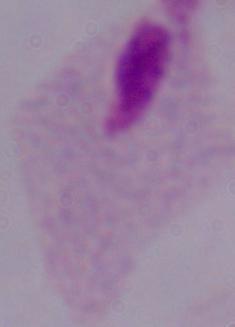
Summary:
  - Magnification: 1000x
  - Identification: trichomonad
  - Modality: micrograph